Locate platelets.
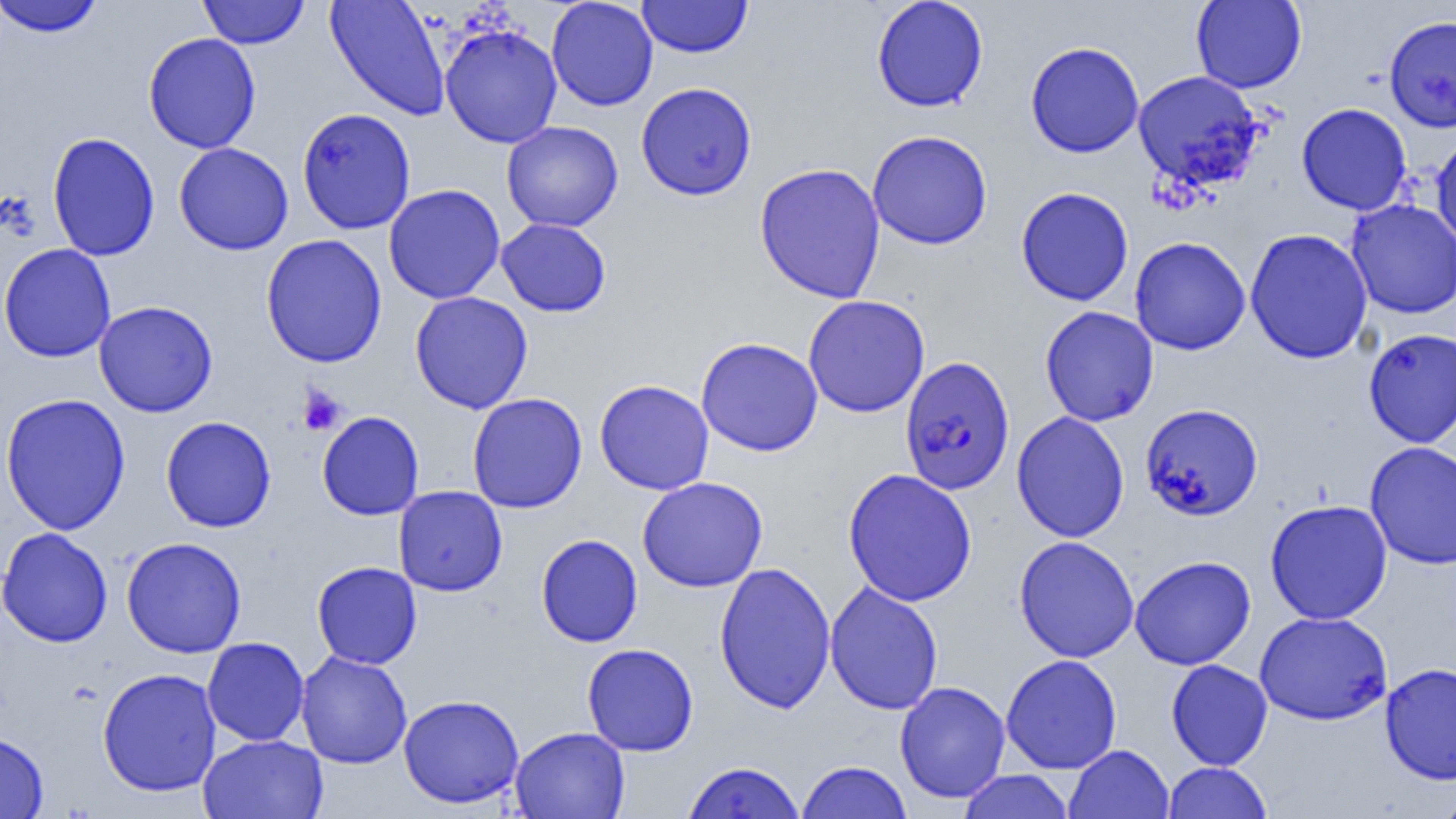
Approximate bounding boxes as named x1/y1/x2/y2 corners in pixels.
Platelets: (x1=297, y1=385, x2=346, y2=435).

Summary:
  - Uninfected red blood cell locations: (x1=0, y1=0, x2=105, y2=37), (x1=198, y1=0, x2=309, y2=49), (x1=325, y1=0, x2=450, y2=121), (x1=546, y1=0, x2=659, y2=111), (x1=637, y1=0, x2=753, y2=58), (x1=871, y1=0, x2=989, y2=112), (x1=1190, y1=0, x2=1307, y2=93), (x1=1384, y1=15, x2=1456, y2=132), (x1=440, y1=23, x2=563, y2=148), (x1=142, y1=32, x2=261, y2=154), (x1=1025, y1=41, x2=1144, y2=158), (x1=1132, y1=70, x2=1265, y2=191), (x1=635, y1=82, x2=757, y2=200), (x1=1296, y1=103, x2=1412, y2=215), (x1=296, y1=107, x2=416, y2=235), (x1=501, y1=121, x2=624, y2=232), (x1=867, y1=130, x2=993, y2=250), (x1=46, y1=131, x2=160, y2=261), (x1=1430, y1=133, x2=1456, y2=248), (x1=173, y1=142, x2=294, y2=255), (x1=754, y1=162, x2=886, y2=303), (x1=383, y1=184, x2=506, y2=305), (x1=1015, y1=187, x2=1134, y2=306), (x1=1346, y1=199, x2=1456, y2=319), (x1=496, y1=218, x2=611, y2=317), (x1=1245, y1=228, x2=1373, y2=364), (x1=260, y1=234, x2=387, y2=368), (x1=1130, y1=236, x2=1251, y2=355), (x1=0, y1=243, x2=116, y2=362), (x1=409, y1=292, x2=533, y2=414), (x1=802, y1=294, x2=930, y2=418), (x1=93, y1=300, x2=218, y2=417), (x1=1040, y1=305, x2=1159, y2=426), (x1=1363, y1=328, x2=1456, y2=447), (x1=696, y1=337, x2=823, y2=457), (x1=594, y1=379, x2=715, y2=495), (x1=1, y1=392, x2=131, y2=535), (x1=466, y1=392, x2=587, y2=514), (x1=1140, y1=402, x2=1264, y2=521), (x1=316, y1=410, x2=424, y2=520), (x1=1011, y1=411, x2=1129, y2=542), (x1=160, y1=415, x2=276, y2=532), (x1=1364, y1=441, x2=1456, y2=570), (x1=843, y1=468, x2=978, y2=607), (x1=637, y1=476, x2=768, y2=592), (x1=393, y1=485, x2=508, y2=596), (x1=1265, y1=499, x2=1393, y2=625), (x1=0, y1=527, x2=113, y2=648), (x1=536, y1=534, x2=643, y2=647), (x1=1014, y1=535, x2=1139, y2=663), (x1=121, y1=537, x2=247, y2=658), (x1=1130, y1=555, x2=1256, y2=670), (x1=311, y1=561, x2=422, y2=669), (x1=713, y1=561, x2=837, y2=714), (x1=824, y1=581, x2=943, y2=715), (x1=1254, y1=611, x2=1393, y2=726), (x1=202, y1=637, x2=309, y2=746), (x1=582, y1=643, x2=698, y2=756), (x1=296, y1=651, x2=413, y2=769), (x1=1001, y1=654, x2=1122, y2=774), (x1=1166, y1=659, x2=1273, y2=770), (x1=1380, y1=662, x2=1456, y2=784), (x1=97, y1=667, x2=222, y2=797), (x1=895, y1=681, x2=1011, y2=803), (x1=398, y1=694, x2=525, y2=809), (x1=510, y1=726, x2=630, y2=819), (x1=0, y1=731, x2=48, y2=819), (x1=198, y1=734, x2=329, y2=819), (x1=1064, y1=744, x2=1174, y2=819), (x1=683, y1=760, x2=805, y2=818), (x1=796, y1=760, x2=912, y2=819), (x1=1163, y1=762, x2=1272, y2=819), (x1=957, y1=770, x2=1074, y2=818), (x1=1434, y1=790, x2=1456, y2=819)
  - Plasmodium falciparum-infected red blood cell locations: (x1=899, y1=356, x2=1016, y2=495)
  - Slide-level diagnosis: Plasmodium falciparum
  - Modality: optical microscopy
  - Preparation: thin blood film
  - Image size: 1456×819 pixels
  - Field of view: single
  - Magnification: 1000x